State which parasite is depicted.
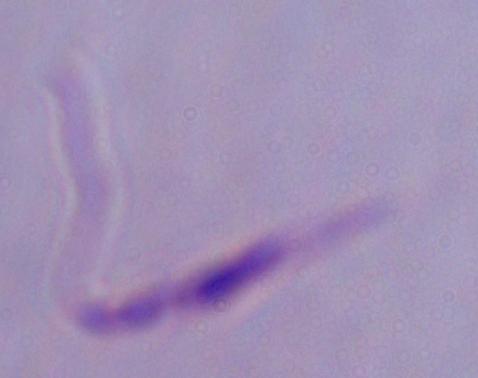
Leishmania.

Summary:
  - Magnification: 1000x
  - Modality: photomicrograph